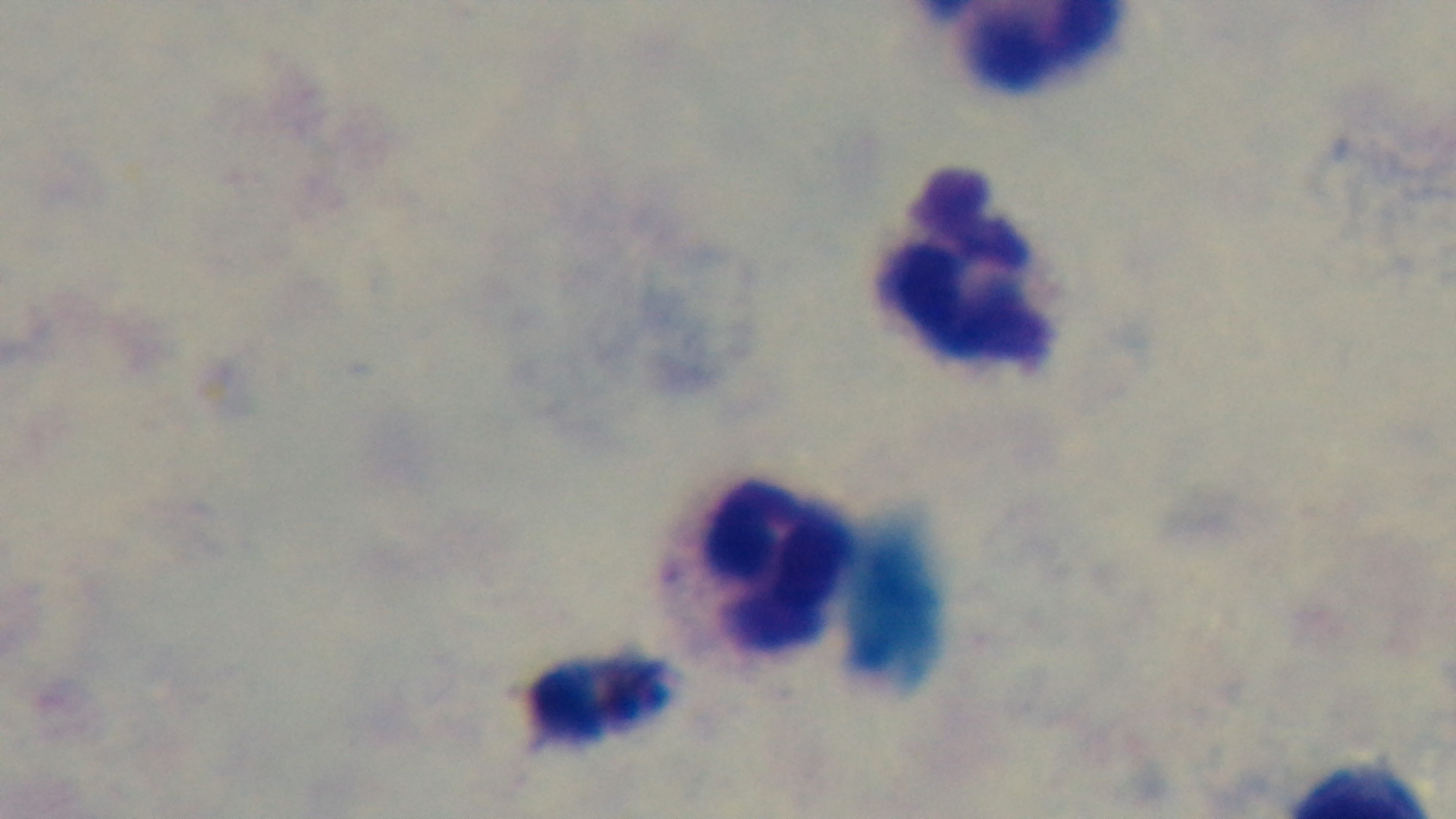

Single field of view. Photomicrograph. Oil-immersion objective, 100x. Malaria status: uninfected. Preparation: thick. Giemsa stain. Captured with a mounted 4K digital camera.